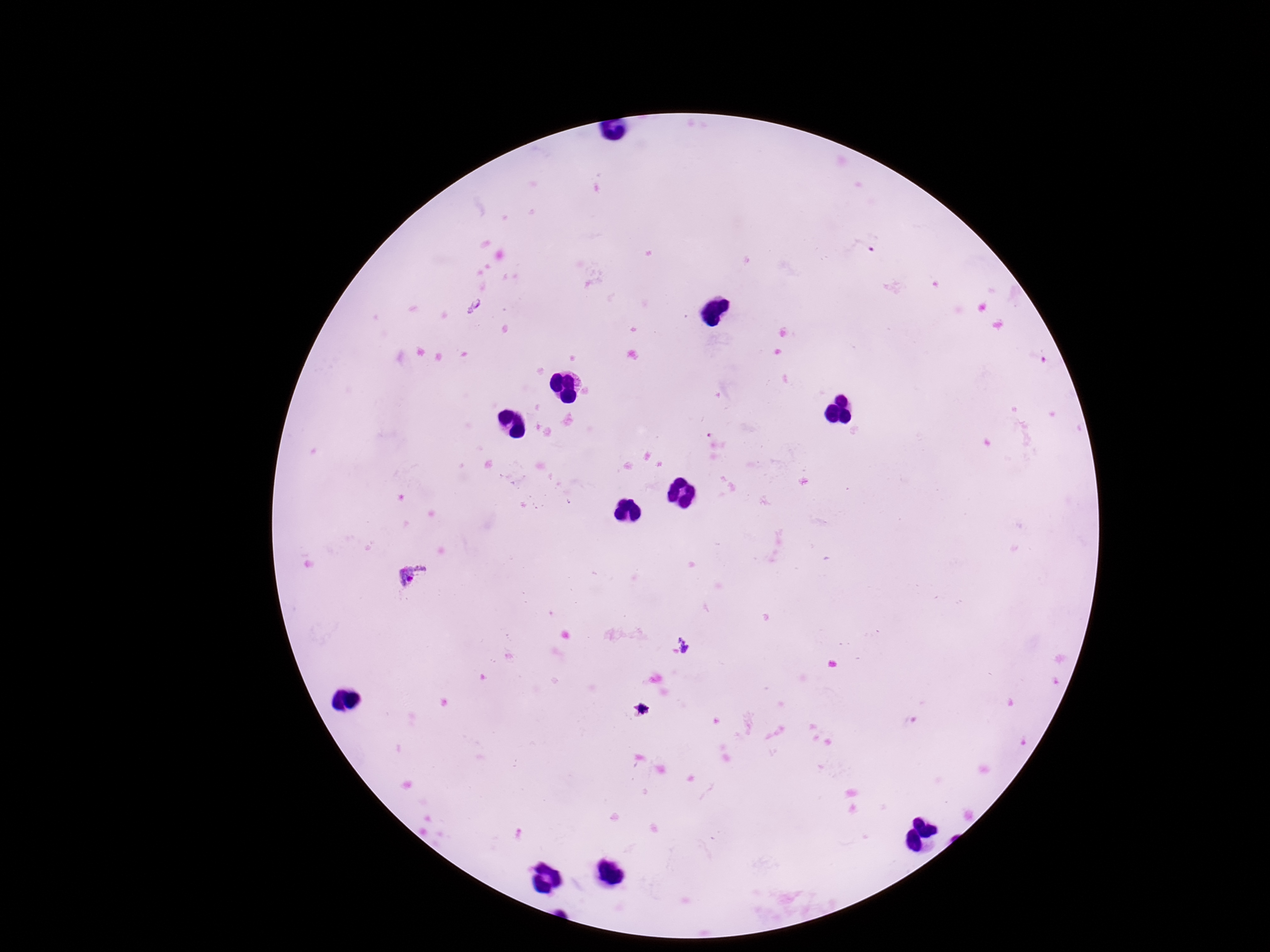
field of view = one from this slide
Plasmodium parasite locations = approximate object centers, in pixels from the top-left corner: (x=413, y=577)
stain = Giemsa
preparation = thick peripheral-blood smear
magnification = 100x
image size = 1270×952 pixels
patient malaria status = positive
capture = smartphone camera through the microscope eyepiece